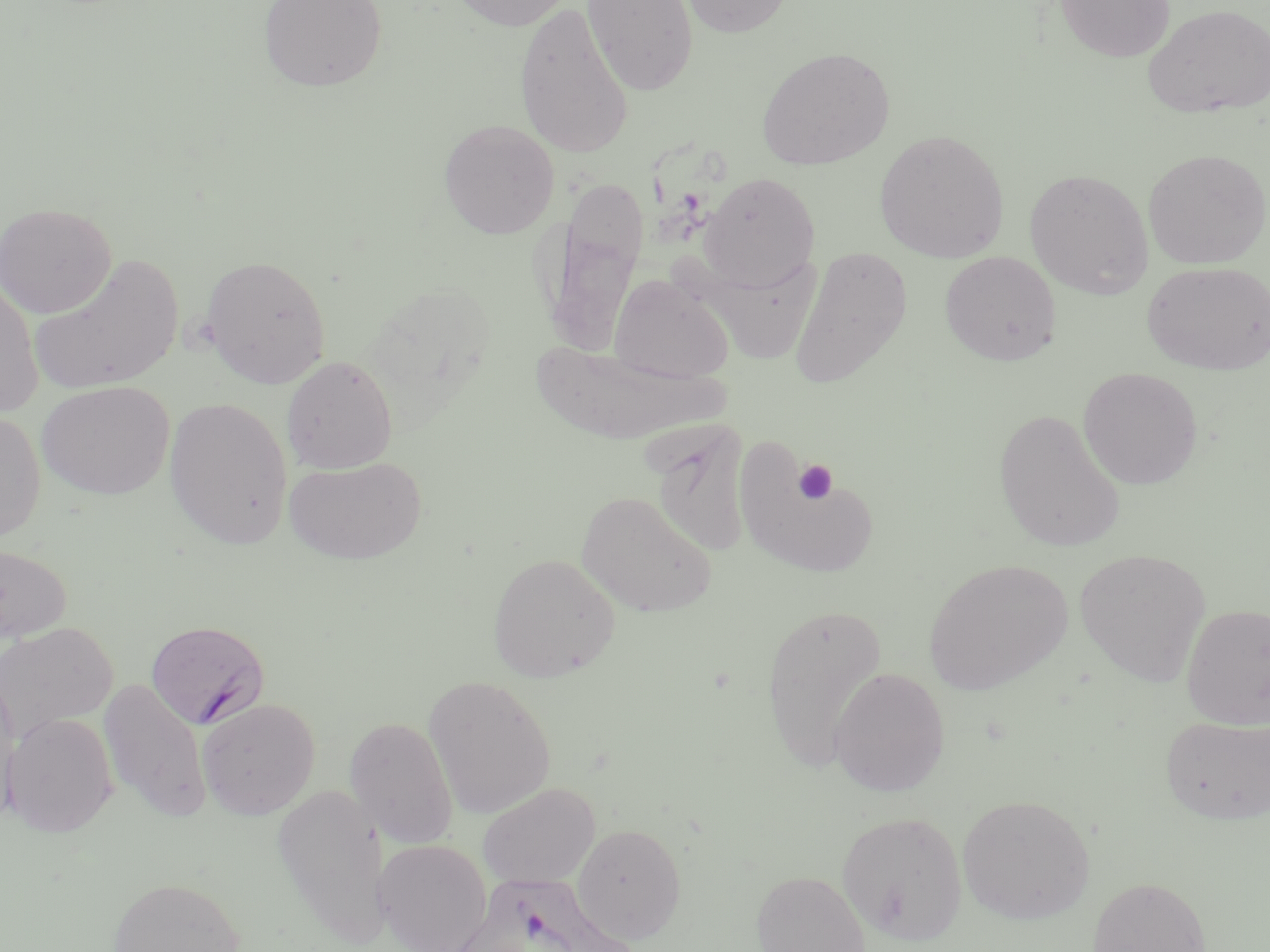

Approximate bounding boxes as [x1, y1, x2, y2] in pixels. Plasmodium falciparum-infected red blood cell locations: [145, 619, 270, 730], [445, 871, 624, 952]. Platelet locations: [792, 460, 838, 504]. Uninfected red blood cell locations: [256, 0, 388, 92], [448, 0, 575, 31], [582, 0, 699, 96], [676, 0, 795, 37], [1054, 0, 1175, 63], [514, 2, 635, 159], [1142, 3, 1270, 118], [757, 46, 895, 170], [439, 119, 559, 238], [874, 128, 1010, 263], [1142, 148, 1270, 269], [1024, 168, 1154, 299], [699, 172, 820, 290], [541, 175, 650, 353], [0, 202, 116, 318], [788, 247, 913, 389], [939, 251, 1061, 367], [29, 253, 184, 397], [200, 254, 331, 389], [1142, 261, 1270, 375], [609, 272, 735, 384], [0, 276, 43, 417], [534, 326, 739, 445], [281, 356, 397, 474], [1078, 367, 1203, 490], [36, 381, 175, 499], [164, 396, 294, 549], [994, 409, 1126, 553], [0, 410, 45, 542], [641, 413, 761, 564], [737, 452, 881, 579], [284, 456, 427, 565], [576, 491, 718, 618], [0, 542, 71, 645], [1075, 548, 1211, 686], [487, 553, 621, 683], [925, 558, 1072, 695], [759, 601, 888, 773], [1181, 603, 1270, 729], [0, 622, 116, 742], [829, 667, 950, 797], [423, 675, 557, 818], [0, 676, 21, 823], [97, 678, 213, 822], [197, 697, 320, 819], [1, 712, 119, 837], [1159, 714, 1270, 825], [343, 716, 458, 849], [477, 782, 600, 890], [272, 784, 390, 941], [956, 793, 1095, 925], [838, 810, 967, 945], [573, 823, 686, 943], [373, 839, 492, 952], [751, 869, 871, 952], [107, 876, 244, 951], [1087, 876, 1210, 952]. Slide-level diagnosis: Plasmodium falciparum. May-Grünwald-Giemsa stain. Single field of view. Image is 1270×952 pixels. Light microscopy. 1000x magnification. Thin blood film.